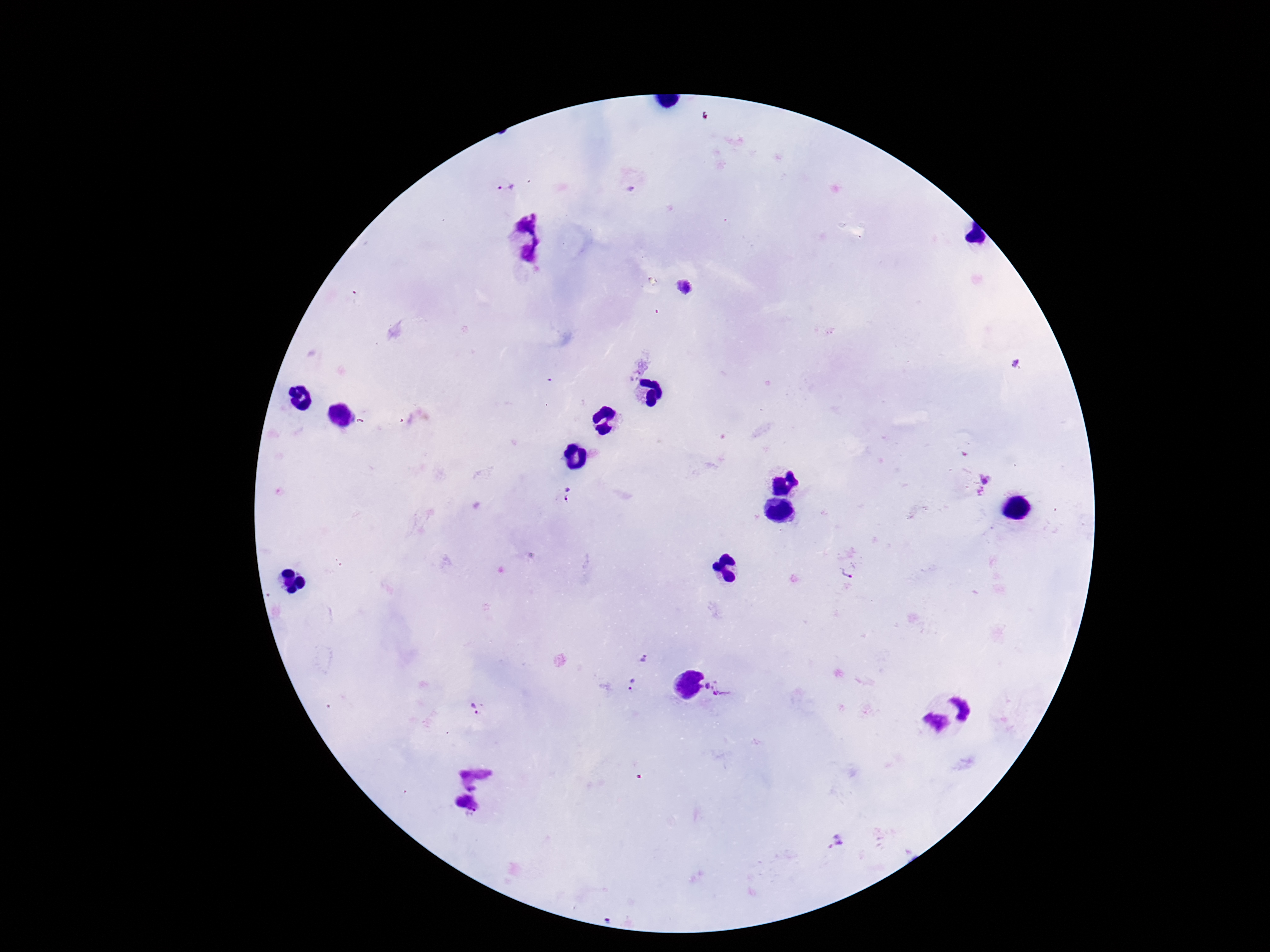

Approximate centers as (x, y) in pixels. Plasmodium parasite locations: (505, 188), (685, 289), (1016, 364), (978, 484), (568, 497), (849, 572), (645, 658), (631, 686), (720, 687), (474, 710), (835, 839). Patient malaria status: positive. Thick peripheral-blood smear. 100x magnification. Giemsa stain. Image is 1270×952 pixels. Smartphone photograph taken through the microscope eyepiece. One field from this slide.